Identify the parasite.
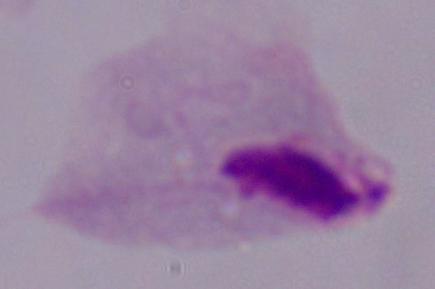
A trichomonad.

{
  "modality": "micrograph",
  "magnification": "1000x"
}